Assess this cell for malaria.
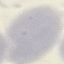
It is uninfected.

stain = Giemsa
image type = automatically extracted cell patch, resized to 64 × 64 pixels
preparation = thin smear
capture = smartphone camera at the microscope eyepiece